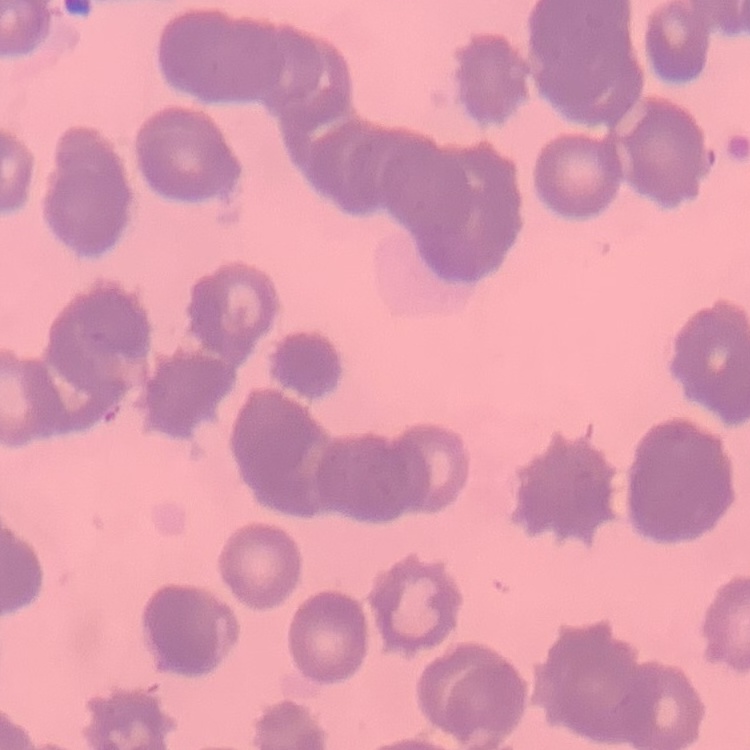

Summary:
  - Red blood cell morphology: rouleaux formation
  - Stain: Field's or Giemsa
  - Image type: one tile cut from a larger photomicrograph
  - Preparation: thin blood smear